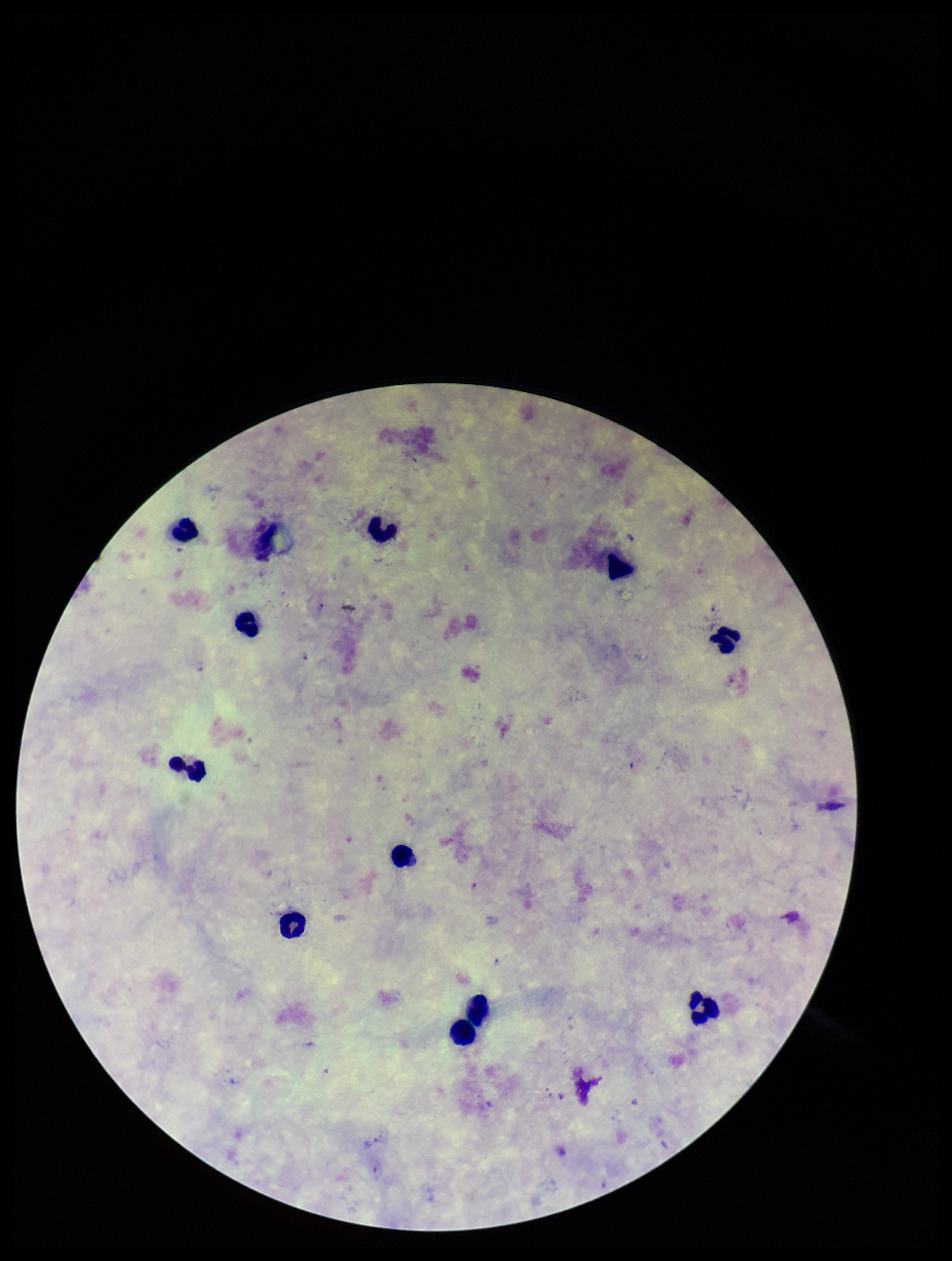

Leukocyte count: 11. Preparation: thick smear. Photographed through the microscope eyepiece with a smartphone camera. One field from this slide. Species reported for this patient: Plasmodium falciparum. Patient malaria status: positive. Image is 952×1261 pixels. Plasmodium parasites: identified. Parasite count: 4. Giemsa stain.